Name the blood parasite species.
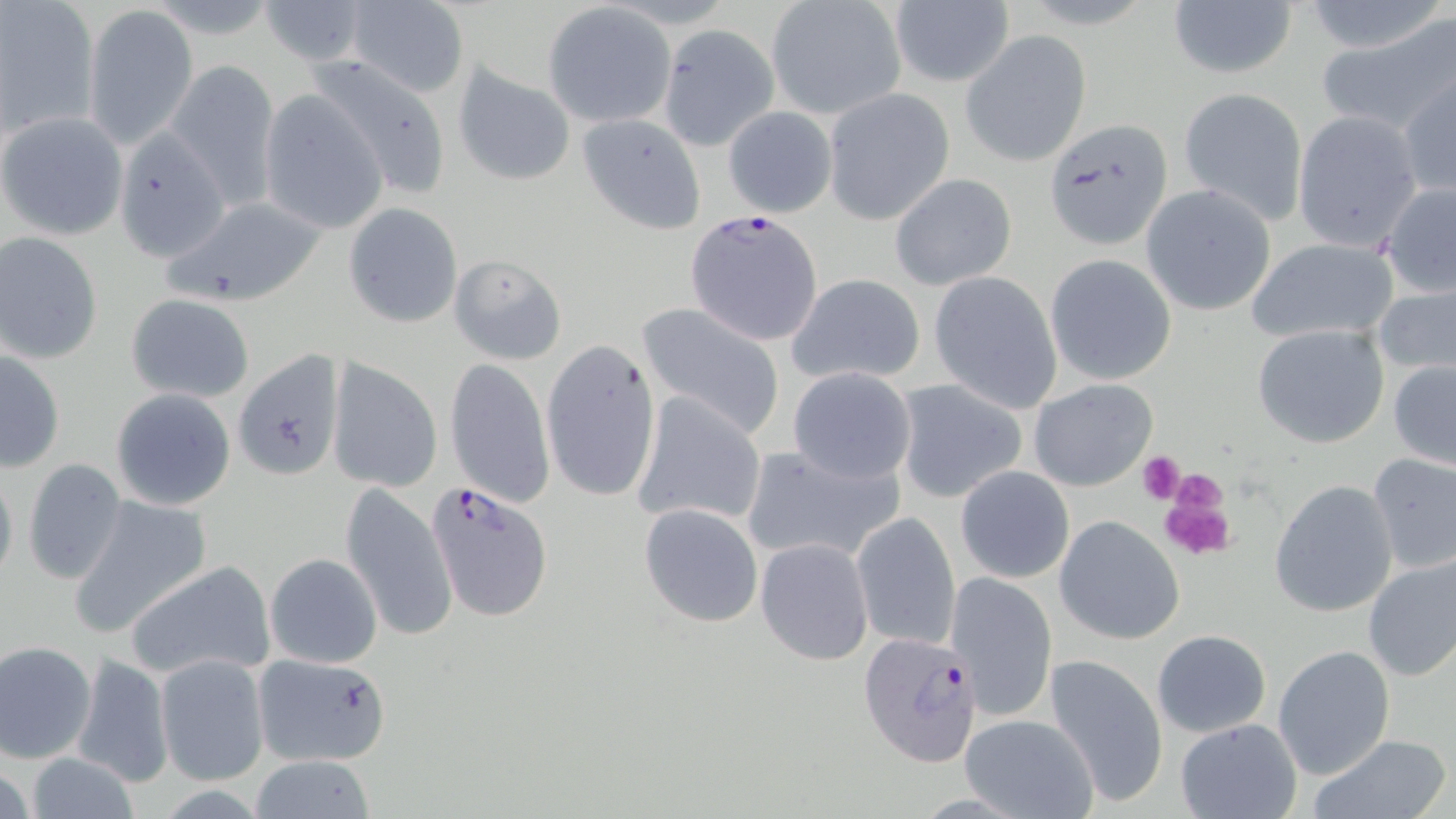

Plasmodium falciparum.

Approximate bounding boxes as [x1, y1, x2, y2] in pixels. Uninfected red blood cell locations: [1, 0, 98, 139], [254, 0, 373, 64], [343, 0, 470, 98], [1300, 0, 1449, 55], [767, 1, 905, 120], [1167, 1, 1297, 80], [890, 2, 1014, 89], [83, 4, 198, 150], [541, 4, 676, 128], [1320, 14, 1456, 139], [658, 23, 779, 151], [961, 31, 1091, 167], [168, 59, 280, 209], [304, 59, 452, 203], [451, 63, 577, 187], [1397, 69, 1456, 201], [1178, 86, 1306, 224], [823, 88, 954, 224], [257, 90, 388, 235], [723, 105, 837, 217], [0, 111, 127, 241], [1291, 111, 1423, 249], [578, 113, 706, 235], [1044, 121, 1174, 251], [112, 132, 229, 262], [888, 172, 1016, 290], [1381, 182, 1456, 298], [1141, 184, 1277, 316], [159, 195, 328, 308], [342, 201, 463, 328], [1, 233, 103, 363], [1246, 237, 1400, 343], [448, 254, 568, 364], [1046, 255, 1177, 386], [928, 271, 1063, 412], [786, 273, 926, 386], [1373, 282, 1456, 381], [124, 293, 256, 403], [636, 302, 785, 439], [1251, 324, 1389, 450], [541, 338, 661, 503], [0, 349, 66, 472], [232, 352, 345, 482], [328, 355, 443, 495], [445, 359, 555, 510], [1388, 359, 1456, 470], [788, 367, 917, 485], [892, 377, 1029, 504], [1028, 377, 1159, 492], [110, 387, 237, 511], [631, 395, 767, 532], [740, 443, 905, 566], [1365, 452, 1456, 574], [21, 458, 128, 585], [0, 461, 18, 592], [955, 467, 1075, 583], [1269, 479, 1399, 618], [339, 482, 456, 644], [67, 494, 214, 639], [639, 504, 762, 628], [849, 510, 960, 654], [1055, 516, 1184, 644], [756, 537, 873, 666], [264, 553, 382, 669], [1361, 553, 1456, 682], [124, 561, 277, 680], [945, 571, 1062, 721], [1152, 630, 1272, 737], [0, 640, 96, 762], [1273, 645, 1396, 780], [255, 647, 390, 772], [71, 652, 173, 788], [155, 654, 270, 785], [1043, 654, 1168, 809], [958, 714, 1099, 819], [1174, 718, 1303, 819], [1305, 733, 1453, 819], [248, 754, 377, 819], [21, 755, 145, 817]. Plasmodium falciparum-infected red blood cell locations: [685, 209, 825, 346], [426, 482, 553, 622], [858, 631, 985, 767]. Platelet locations: [1138, 453, 1187, 503], [1166, 467, 1229, 520], [1158, 492, 1237, 561]. Light microscopy. Captured at 1000x magnification. May-Grünwald-Giemsa-stained preparation. Single field of view. Image is 1456×819 pixels. Thin blood film.